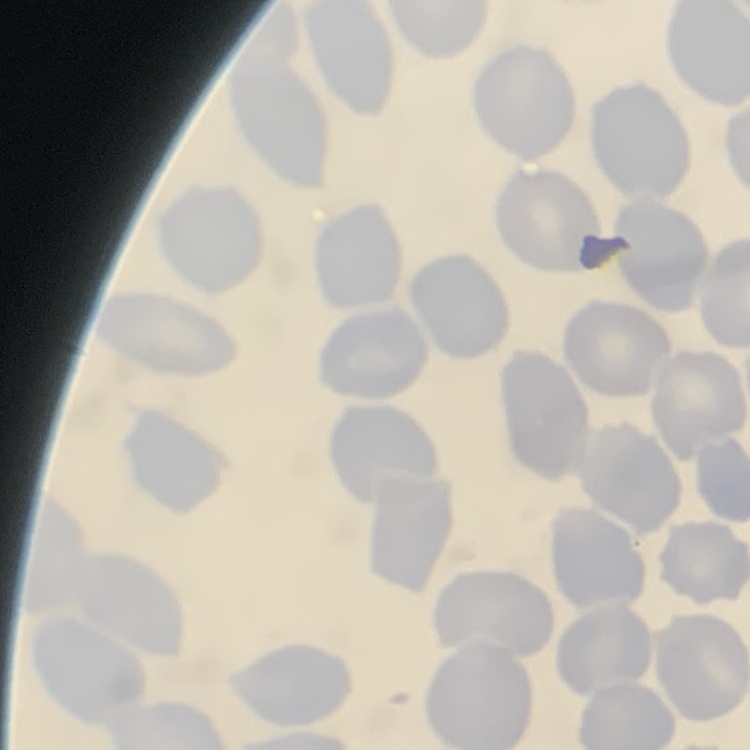

erythrocyte morphology = no rouleaux formation
image type = one tile cut from a larger photomicrograph
preparation = thin peripheral smear
stain = Field's or Giemsa